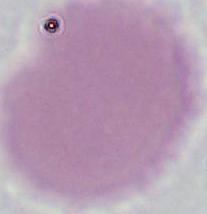

identification = red blood cell
magnification = 1000x
modality = photomicrograph